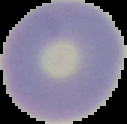
image size = 127×124 pixels
result = no malaria parasites detected
image type = segmented cell region with the area outside set to black
preparation = thin blood smear